Report the malaria status of this cell.
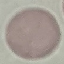
It is uninfected.

{
  "image_type": "automatically extracted cell patch, resized to 64 × 64 pixels",
  "preparation": "thin blood smear",
  "stain": "Giemsa",
  "capture": "smartphone camera at the microscope eyepiece"
}